Locate and identify every blood parasite.
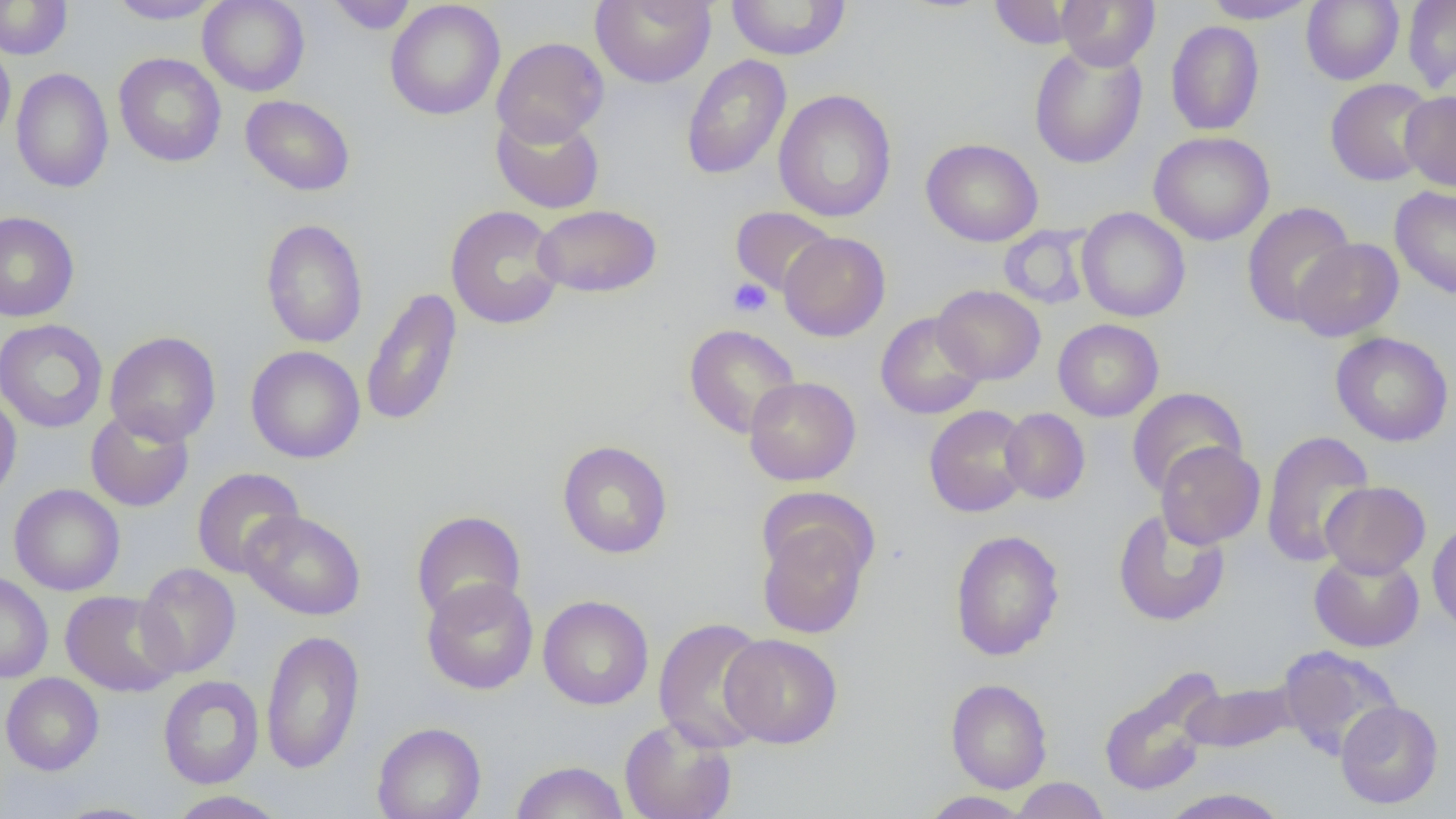

No blood parasites seen.

Approximate bounding boxes as (x1,y1)-(x2,y2) corner pairs in pixels. Platelet locations: (728,278)-(772,317). Uninfected red blood cell locations: (107,0)-(222,24), (197,0)-(310,96), (591,0)-(716,87), (725,0)-(852,60), (1056,0)-(1160,70), (1202,0)-(1318,23), (1301,0)-(1404,85), (1402,0)-(1456,94), (0,1)-(73,59), (326,1)-(418,34), (385,1)-(505,120), (987,1)-(1085,49), (1166,21)-(1265,136), (492,37)-(609,146), (0,39)-(15,146), (1029,42)-(1147,169), (114,52)-(227,167), (681,54)-(792,180), (11,68)-(114,193), (1325,78)-(1436,186), (774,89)-(897,223), (1399,91)-(1456,191), (240,94)-(356,196), (491,109)-(604,214), (1149,131)-(1274,245), (921,138)-(1043,246), (1390,185)-(1456,299), (1241,201)-(1357,327), (445,204)-(565,330), (533,204)-(662,298), (730,206)-(836,296), (1076,207)-(1191,322), (0,211)-(80,322), (260,218)-(368,349), (998,224)-(1093,310), (779,231)-(891,341), (1291,238)-(1404,341), (933,285)-(1045,384), (361,287)-(462,427), (875,312)-(987,420), (0,319)-(109,433), (1053,319)-(1163,422), (684,324)-(801,439), (104,331)-(221,445), (1330,332)-(1454,447), (246,345)-(366,463), (744,376)-(861,486), (1126,387)-(1246,497), (0,392)-(22,504), (924,405)-(1032,517), (85,407)-(194,512), (1000,408)-(1090,504), (1260,430)-(1376,568), (557,440)-(673,559), (1155,441)-(1265,548), (191,467)-(305,578), (1320,481)-(1430,578), (9,484)-(125,596), (1112,509)-(1231,627), (239,510)-(367,620), (411,510)-(527,624), (757,517)-(874,640), (1427,521)-(1456,636), (950,530)-(1065,661), (1309,551)-(1424,652), (134,563)-(241,677), (0,571)-(53,683), (422,577)-(539,695), (60,590)-(183,697), (538,595)-(654,710), (653,617)-(773,754), (260,628)-(365,775), (719,633)-(843,748), (1277,645)-(1402,761), (1097,669)-(1221,797), (1,672)-(104,775), (158,675)-(264,789), (945,679)-(1052,793), (1180,680)-(1299,754), (1335,700)-(1444,809), (620,717)-(737,819), (371,722)-(486,819), (510,760)-(630,819), (1010,777)-(1110,819), (1159,788)-(1291,818), (165,790)-(290,819), (920,791)-(1034,818), (49,802)-(163,818). Slide-level diagnosis: no evidence of blood parasites. Optical microscopy. Image is 1456×819 pixels. Thin blood smear. One field of a larger specimen. 1000x magnification.